Locate every Plasmodium vivax-infected red blood cell.
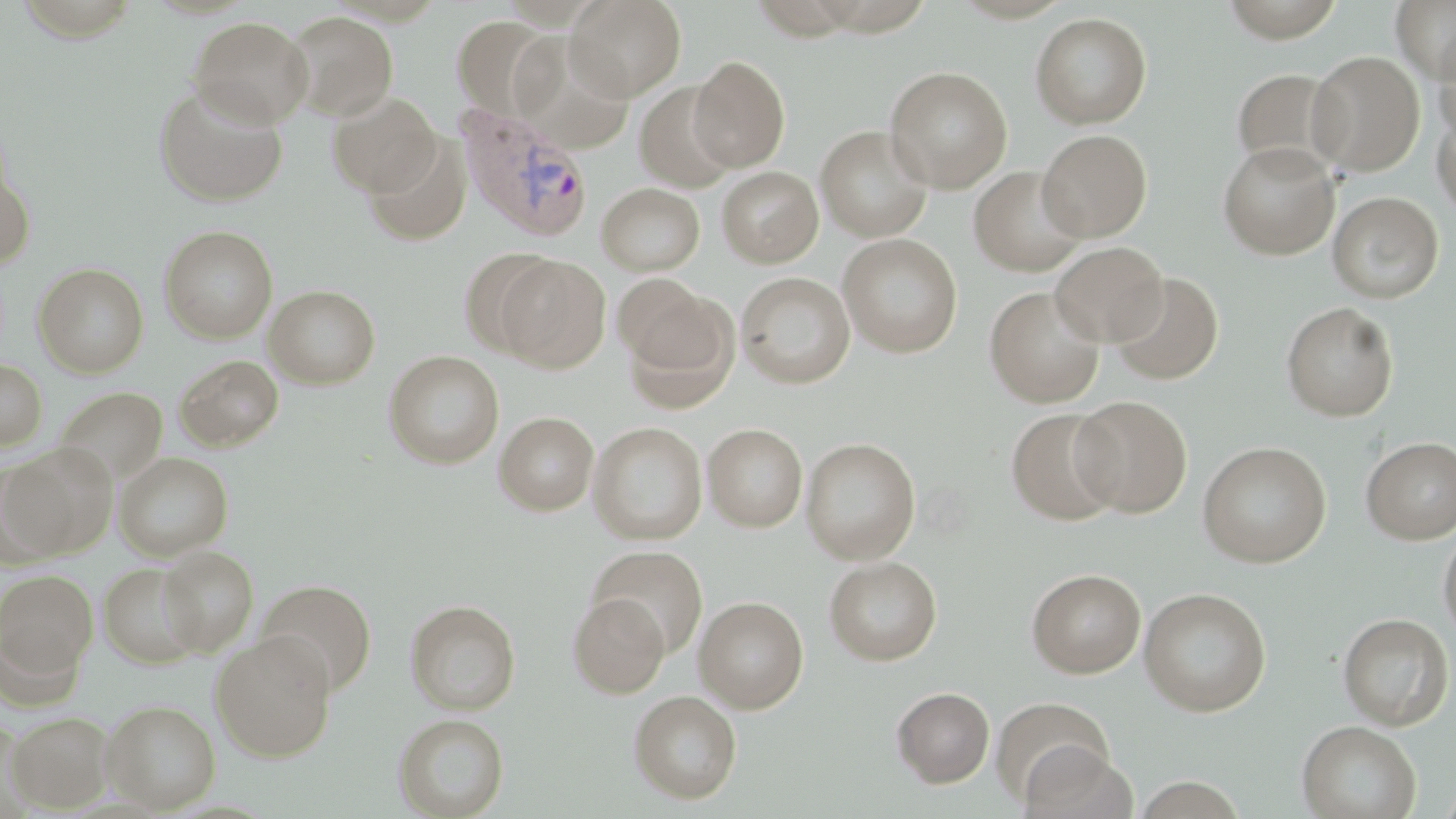
Approximate bounding boxes as (x1,y1)-(x2,y2) corner pairs in pixels.
Plasmodium vivax-infected red blood cells: (458,107)-(594,241).

Summary:
  - Uninfected red blood cell locations: (566,0)-(687,101), (1217,0)-(1347,42), (1391,0)-(1456,85), (284,11)-(399,121), (1030,12)-(1152,129), (189,16)-(313,127), (452,16)-(557,120), (516,28)-(637,150), (1434,31)-(1456,147), (1306,50)-(1426,177), (688,56)-(791,172), (884,65)-(1012,193), (1231,67)-(1345,176), (635,82)-(738,193), (153,83)-(289,207), (327,91)-(441,198), (1432,102)-(1455,220), (815,125)-(934,242), (1037,129)-(1152,241), (364,134)-(472,245), (1217,141)-(1340,260), (0,161)-(35,271), (717,166)-(823,267), (968,166)-(1088,276), (597,183)-(705,276), (1328,191)-(1444,304), (159,225)-(278,343), (837,233)-(963,358), (1050,241)-(1168,347), (459,247)-(560,360), (496,255)-(611,373), (33,262)-(149,378), (1108,271)-(1225,385), (736,272)-(855,388), (614,273)-(715,368), (264,285)-(380,389), (984,285)-(1106,408), (627,295)-(741,413), (1281,301)-(1399,421), (383,350)-(504,469), (174,355)-(283,451), (0,359)-(47,452), (53,386)-(168,486), (1070,395)-(1192,518), (1006,408)-(1123,525), (494,411)-(599,515), (588,422)-(707,545), (703,423)-(808,532), (1360,436)-(1456,545), (800,437)-(920,564), (1197,441)-(1331,567), (3,444)-(117,561), (115,452)-(233,560), (1438,525)-(1456,646), (157,546)-(258,657), (589,546)-(709,658), (823,556)-(942,666), (99,563)-(204,668), (1027,568)-(1146,678), (0,569)-(98,680), (256,579)-(377,695), (1138,587)-(1272,716), (568,594)-(671,697), (694,596)-(809,713), (405,599)-(521,715), (1337,612)-(1454,730), (210,632)-(337,762), (891,686)-(995,788), (628,691)-(742,804), (991,698)-(1115,806), (102,699)-(220,813), (6,711)-(116,813), (393,714)-(509,818), (1296,720)-(1420,819), (1021,744)-(1136,819), (1436,779)-(1456,818)
  - Slide-level diagnosis: Plasmodium vivax
  - Image size: 1456×819 pixels
  - Field of view: one of a larger specimen
  - Preparation: thin blood film
  - Magnification: 1000x
  - Stain: May-Grünwald-Giemsa
  - Modality: light microscopy